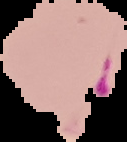

Image is 127×142 pixels. Cell region segmented out of the field of view; the surrounding area is masked to black. From a thin blood film. Malaria status: parasitized.